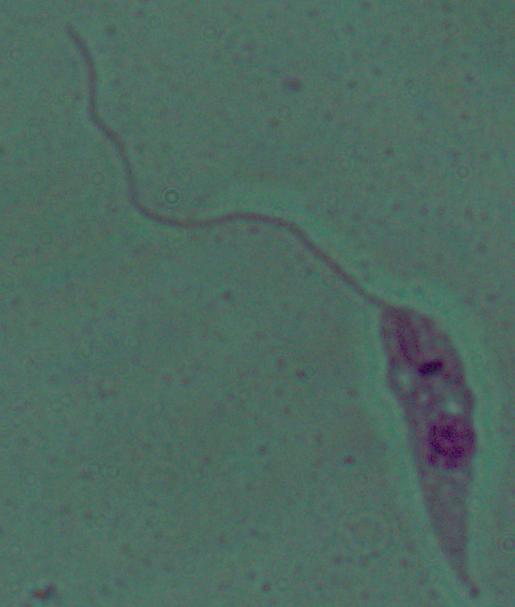

Summary:
  - Magnification: 1000x
  - Modality: photomicrograph
  - Identification: Leishmania